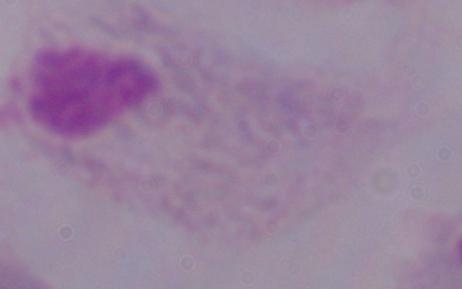 1000x magnification. A trichomonad is shown. Photomicrograph.